Describe the morphology of the erythrocytes.
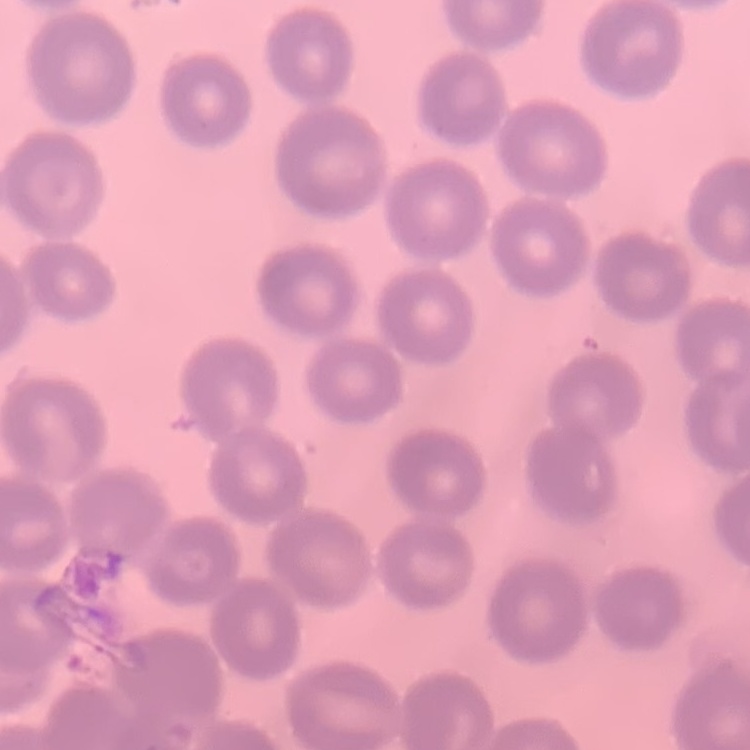

No rouleaux formation.

image type = one tile cut from a larger photomicrograph
stain = Field's or Giemsa
preparation = thin peripheral smear